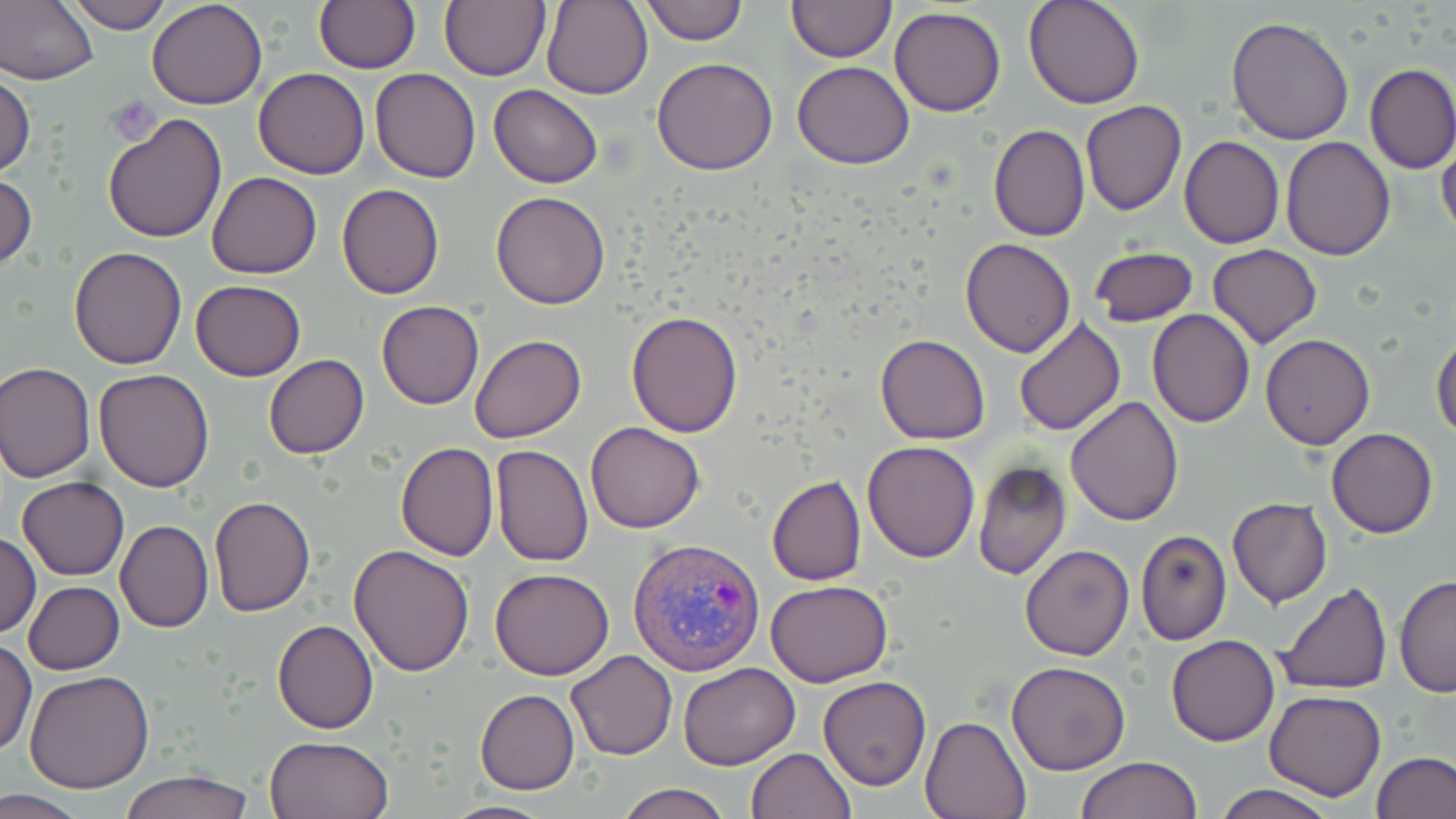

Approximate bounding boxes as [x1, y1, x2, y2] in pixels. Plasmodium vivax-infected red blood cell locations: [630, 537, 765, 674]. Platelet locations: [107, 96, 158, 144]. Uninfected red blood cell locations: [61, 0, 173, 34], [147, 0, 268, 110], [439, 0, 550, 81], [540, 0, 652, 99], [787, 0, 895, 62], [1023, 0, 1146, 110], [1, 1, 99, 88], [314, 1, 421, 74], [638, 1, 747, 44], [889, 6, 1006, 117], [1226, 17, 1354, 145], [651, 56, 778, 175], [792, 60, 915, 169], [1365, 64, 1456, 174], [253, 68, 371, 179], [370, 68, 481, 183], [0, 70, 35, 177], [489, 84, 602, 188], [1080, 101, 1187, 217], [102, 112, 229, 244], [989, 124, 1091, 241], [1179, 136, 1285, 249], [1280, 137, 1395, 260], [1436, 139, 1456, 242], [206, 171, 323, 278], [0, 172, 37, 273], [336, 183, 444, 300], [491, 192, 609, 309], [959, 238, 1076, 357], [1209, 244, 1322, 348], [68, 246, 189, 368], [1085, 246, 1198, 328], [190, 279, 306, 381], [376, 300, 485, 409], [1146, 308, 1256, 428], [626, 310, 744, 436], [1011, 318, 1127, 437], [1431, 332, 1456, 439], [875, 333, 990, 445], [1260, 333, 1374, 450], [470, 334, 586, 444], [263, 355, 368, 459], [0, 362, 96, 482], [94, 369, 215, 492], [1065, 395, 1185, 524], [585, 421, 705, 533], [1326, 429, 1439, 538], [861, 440, 980, 563], [395, 442, 498, 561], [490, 443, 592, 567], [973, 460, 1072, 580], [766, 476, 865, 585], [17, 477, 128, 580], [209, 496, 315, 617], [1227, 498, 1332, 608], [114, 519, 214, 633], [1135, 529, 1231, 645], [1, 531, 40, 639], [349, 543, 474, 677], [1020, 543, 1136, 660], [490, 567, 615, 679], [1395, 575, 1456, 696], [767, 580, 893, 687], [1274, 580, 1394, 698], [24, 581, 124, 674], [272, 621, 378, 733], [1167, 635, 1279, 747], [0, 637, 37, 755], [568, 650, 677, 760], [1006, 660, 1130, 775], [677, 661, 801, 769], [24, 670, 155, 792], [818, 675, 931, 790], [476, 689, 579, 794], [1264, 689, 1385, 800], [921, 716, 1031, 819], [264, 735, 394, 819], [746, 747, 856, 818], [1373, 752, 1454, 819], [1076, 756, 1203, 819], [118, 770, 254, 819], [615, 782, 732, 819], [1210, 783, 1341, 819], [0, 790, 93, 818], [441, 799, 558, 818]. Slide-level diagnosis: Plasmodium vivax. Optical microscopy. May-Grünwald-Giemsa stain. Single field of view. Image is 1456×819 pixels. Thin blood smear. 1000x magnification.